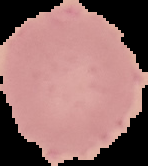
{
  "image_size": "148×166 pixels",
  "result": "no malaria parasites detected",
  "image_type": "segmented cell region with the area outside set to black",
  "preparation": "thin blood film"
}